State which parasite is depicted.
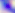

This is Toxoplasma gondii.

400x magnification. Photomicrograph.